Classify this cell by malaria status.
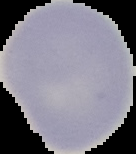
Uninfected.

Cell region segmented out of the field of view; the surrounding area is masked to black. From a thin blood smear. Image is 136×154 pixels.